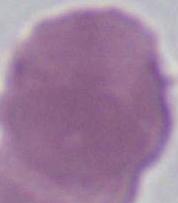

Summary:
  - Identification: red blood cell
  - Magnification: 1000x
  - Modality: micrograph